Give the position of every malaria parasite and every leukocyte.
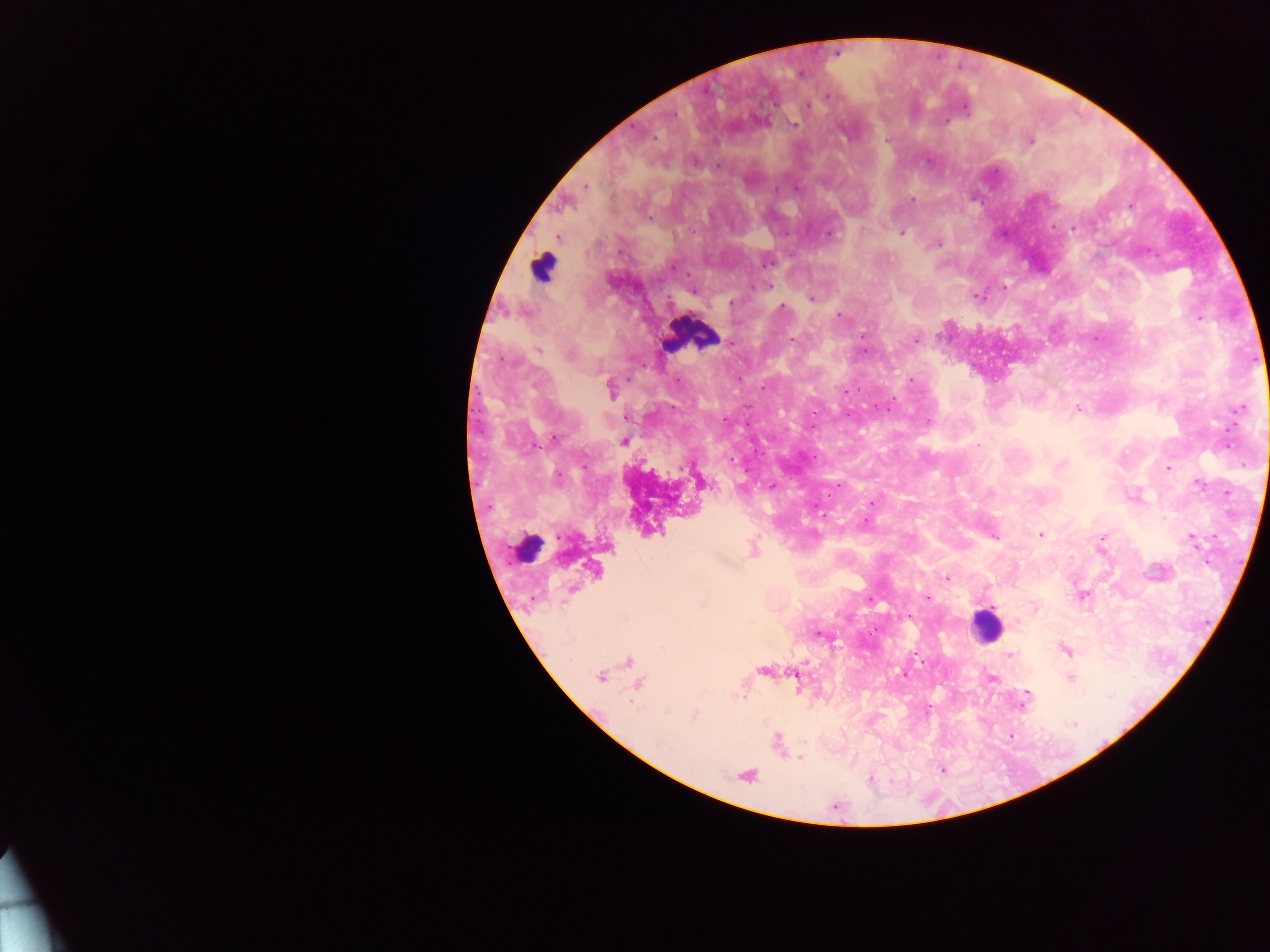
Approximate centers as x y in pixels.
Malaria parasites: 836 55; 707 90; 826 99; 776 102; 963 106; 808 107; 676 115; 794 121; 944 123; 631 126; 655 137; 886 137; 1031 140; 927 162; 717 166; 989 176; 797 185; 585 186; 912 199; 1130 205; 650 219; 1074 224; 1052 226; 692 229; 787 233; 830 233; 900 234; 1004 234; 941 242; 1148 251; 768 262; 672 268; 688 274; 767 285; 753 287; 1004 287; 695 292; 977 296; 667 297; 812 298; 729 304; 780 308; 839 316; 1199 317; 863 334; 793 339; 1095 339; 916 340; 732 342; 866 349; 1254 360; 501 361; 645 366; 740 378; 629 380; 679 380; 912 381; 762 388; 858 391; 846 392; 894 398; 1244 404; 1077 406; 877 407; 673 408; 1235 410; 814 412; 888 412; 848 416; 625 417; 928 423; 748 425; 1235 425; 812 427; 1225 430; 554 438; 1227 446; 541 448; 816 454; 733 459; 1243 465; 586 467; 1167 469; 746 471; 558 473; 839 484; 1200 485; 770 487; 829 496; 868 505; 815 508; 823 516; 865 521; 1040 535; 1214 536; 994 537; 1102 537; 558 538; 1187 539; 509 546; 651 558; 509 563; 945 578; 925 596; 531 598; 870 598; 1083 598; 909 616; 876 629; 817 632; 870 633; 914 654; 1013 655; 923 662; 904 673; 1028 693; 743 697; 930 707; 1073 725; 1011 734; 799 758; 869 778.
Leukocytes: 543 264; 688 338; 527 545; 987 627.

capture = mobile-phone photograph through a microscope
preparation = thick blood smear
field of view = single
image size = 1270×952 pixels
country = Ghana